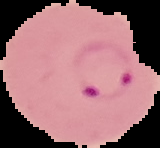

result = Plasmodium parasites identified
preparation = thin blood film
image size = 160×148 pixels
image type = cell region segmented out of the field of view; surrounding area masked to black